Identify the blood parasite species.
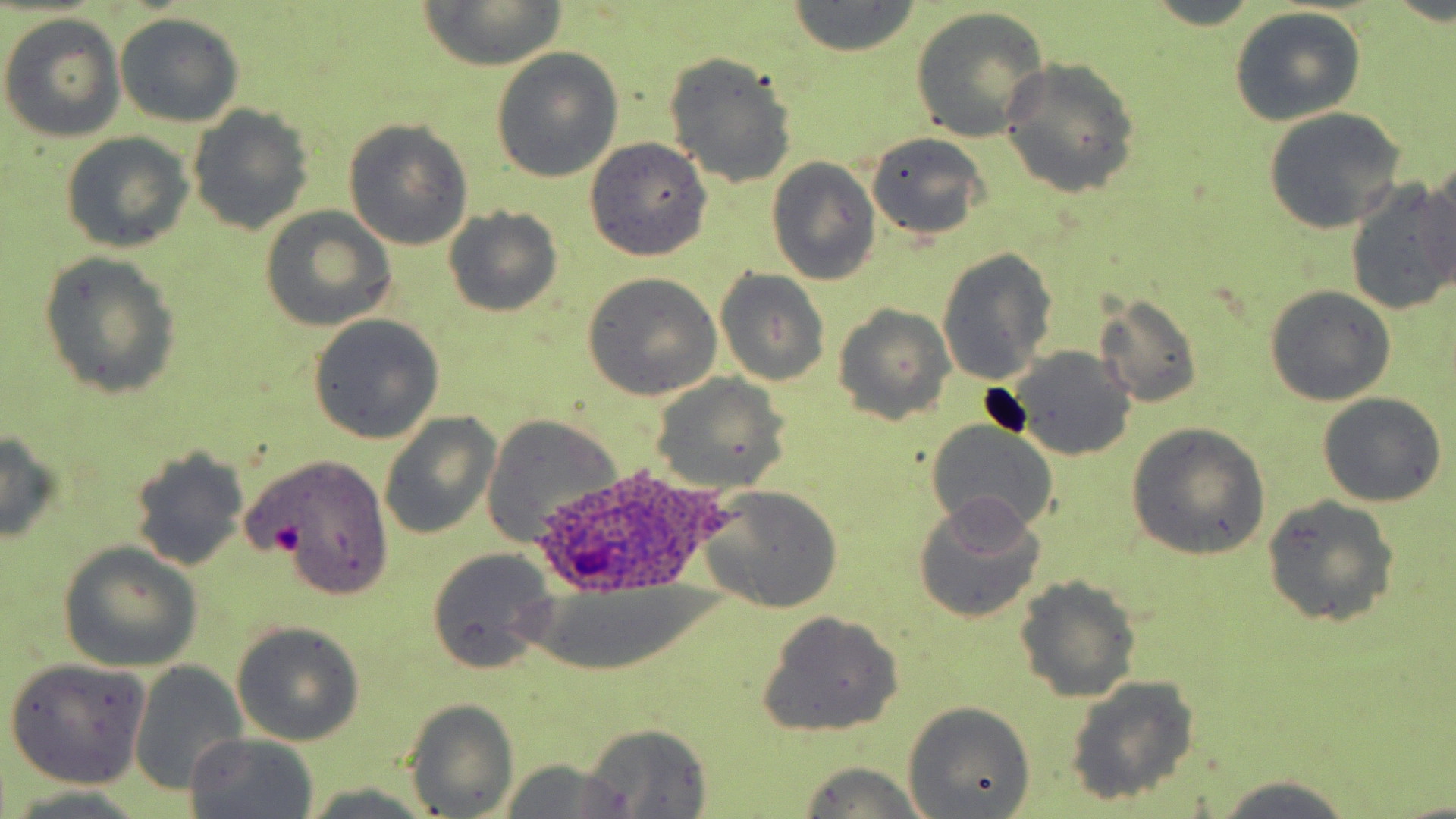

Plasmodium ovale.

Summary:
  - Coordinate format: approximate bounding boxes as (x1,y1)-(x2,y2) corner pairs in pixels
  - Plasmodium ovale-infected red blood cell locations: (532,462)-(721,595)
  - Uninfected red blood cell locations: (421,1)-(566,69), (785,3)-(921,56), (911,8)-(1048,144), (1228,10)-(1366,127), (116,12)-(243,129), (1,13)-(128,143), (490,48)-(624,182), (663,52)-(798,188), (998,59)-(1141,198), (185,105)-(314,235), (1263,108)-(1407,233), (342,119)-(474,251), (60,131)-(194,253), (863,133)-(990,239), (584,138)-(713,262), (766,158)-(881,286), (1408,169)-(1456,305), (1346,179)-(1454,315), (443,205)-(565,318), (259,208)-(398,331), (935,248)-(1058,386), (39,252)-(182,400), (714,269)-(830,387), (580,272)-(724,400), (1265,285)-(1396,405), (1096,295)-(1204,408), (830,304)-(956,425), (309,315)-(443,445), (1001,345)-(1138,462), (648,375)-(788,492), (1319,392)-(1447,508), (378,412)-(501,540), (482,416)-(621,545), (923,418)-(1059,537), (1127,423)-(1270,561), (0,429)-(65,545), (127,446)-(250,571), (251,454)-(396,600), (696,485)-(844,613), (1263,495)-(1399,628), (912,496)-(1050,623), (59,545)-(202,671), (423,549)-(559,673), (1013,578)-(1142,703), (755,611)-(905,737), (232,623)-(365,746), (4,657)-(151,789), (128,660)-(247,797), (1064,675)-(1202,806), (405,699)-(518,817), (902,701)-(1036,816), (578,724)-(714,816), (183,733)-(319,818), (498,757)-(635,819), (792,763)-(938,818), (1208,775)-(1355,818), (297,786)-(439,819)
  - Platelet locations: (270,520)-(305,555)
  - Magnification: 1000x
  - Preparation: thin blood smear
  - Modality: optical microscopy
  - Field of view: single
  - Stain: May-Grünwald-Giemsa
  - Image size: 1456×819 pixels